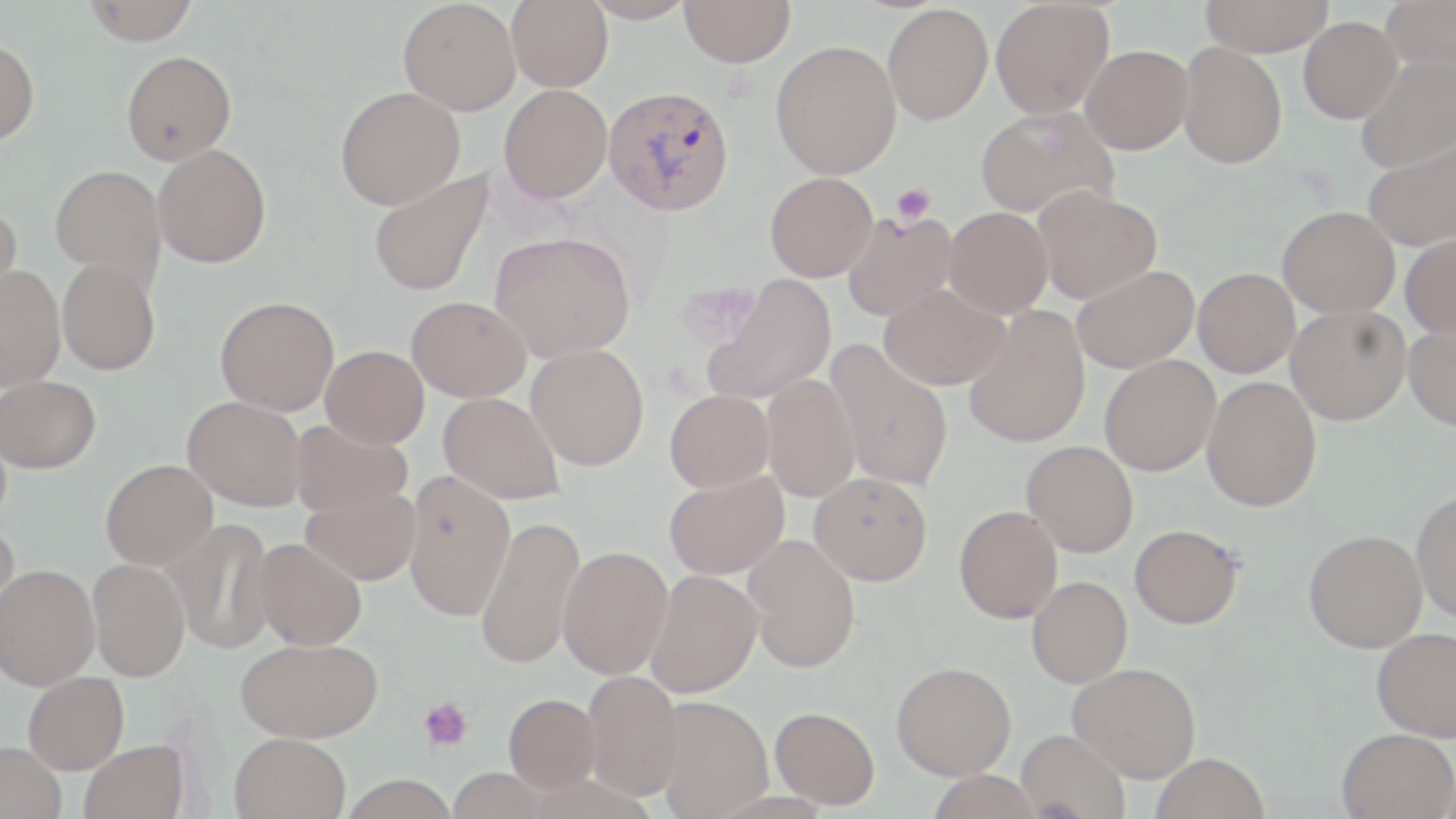

Summary:
  - Coordinate format: approximate bounding boxes as (x1,y1)-(x2,y2) corner pairs in pixels
  - Uninfected red blood cell locations: (82,0)-(200,44), (398,0)-(521,115), (507,0)-(612,91), (582,0)-(696,24), (680,0)-(796,67), (990,0)-(1114,119), (1200,0)-(1334,56), (1380,0)-(1456,73), (883,4)-(993,125), (1298,17)-(1401,123), (0,38)-(40,146), (770,40)-(901,179), (1178,42)-(1287,169), (1080,44)-(1193,154), (121,50)-(236,165), (1354,56)-(1456,172), (499,84)-(612,203), (335,86)-(465,209), (975,106)-(1117,219), (1361,135)-(1456,250), (152,143)-(271,268), (50,165)-(166,287), (369,171)-(494,296), (765,172)-(878,281), (1033,185)-(1161,303), (0,201)-(24,314), (1277,206)-(1400,318), (944,207)-(1053,317), (842,210)-(958,321), (489,232)-(635,362), (1400,233)-(1456,339), (57,258)-(160,375), (1071,265)-(1198,373), (0,266)-(65,390), (1192,268)-(1299,377), (703,276)-(836,404), (879,283)-(1009,389), (215,295)-(339,415), (406,296)-(530,402), (1285,305)-(1411,425), (963,307)-(1091,448), (1404,323)-(1456,430), (825,341)-(954,492), (526,343)-(649,471), (321,345)-(429,448), (1099,355)-(1220,476), (1,374)-(101,473), (761,374)-(860,502), (1201,376)-(1322,511), (665,390)-(775,492), (438,392)-(564,504), (183,396)-(306,511), (290,419)-(412,518), (1021,440)-(1138,557), (100,458)-(217,568), (403,471)-(514,621), (810,471)-(932,585), (664,472)-(789,580), (300,484)-(421,586), (1411,489)-(1456,622), (954,505)-(1063,623), (475,515)-(584,669), (166,518)-(276,654), (0,523)-(20,630), (1129,524)-(1243,629), (1303,529)-(1427,653), (743,534)-(861,673), (250,538)-(367,650), (558,545)-(674,679), (87,557)-(190,682), (0,564)-(100,690), (647,570)-(763,698), (1026,576)-(1132,688), (1371,627)-(1456,741), (235,637)-(383,742), (891,661)-(1016,780), (1067,662)-(1201,782), (582,671)-(686,799), (23,672)-(129,774), (504,693)-(600,792), (651,695)-(773,817), (770,706)-(880,809), (1015,728)-(1130,818), (1336,728)-(1456,819), (229,732)-(351,819), (79,739)-(190,819), (0,742)-(67,819), (1152,753)-(1270,819), (340,775)-(459,819)
  - Platelet locations: (891,183)-(935,224), (418,696)-(474,752)
  - Plasmodium vivax-infected red blood cell locations: (603,85)-(734,216)
  - Slide-level diagnosis: Plasmodium vivax
  - Image size: 1456×819 pixels
  - Magnification: 1000x
  - Field of view: one of a larger specimen
  - Preparation: thin blood smear
  - Modality: light microscopy
  - Stain: May-Grünwald-Giemsa